Report the malaria status.
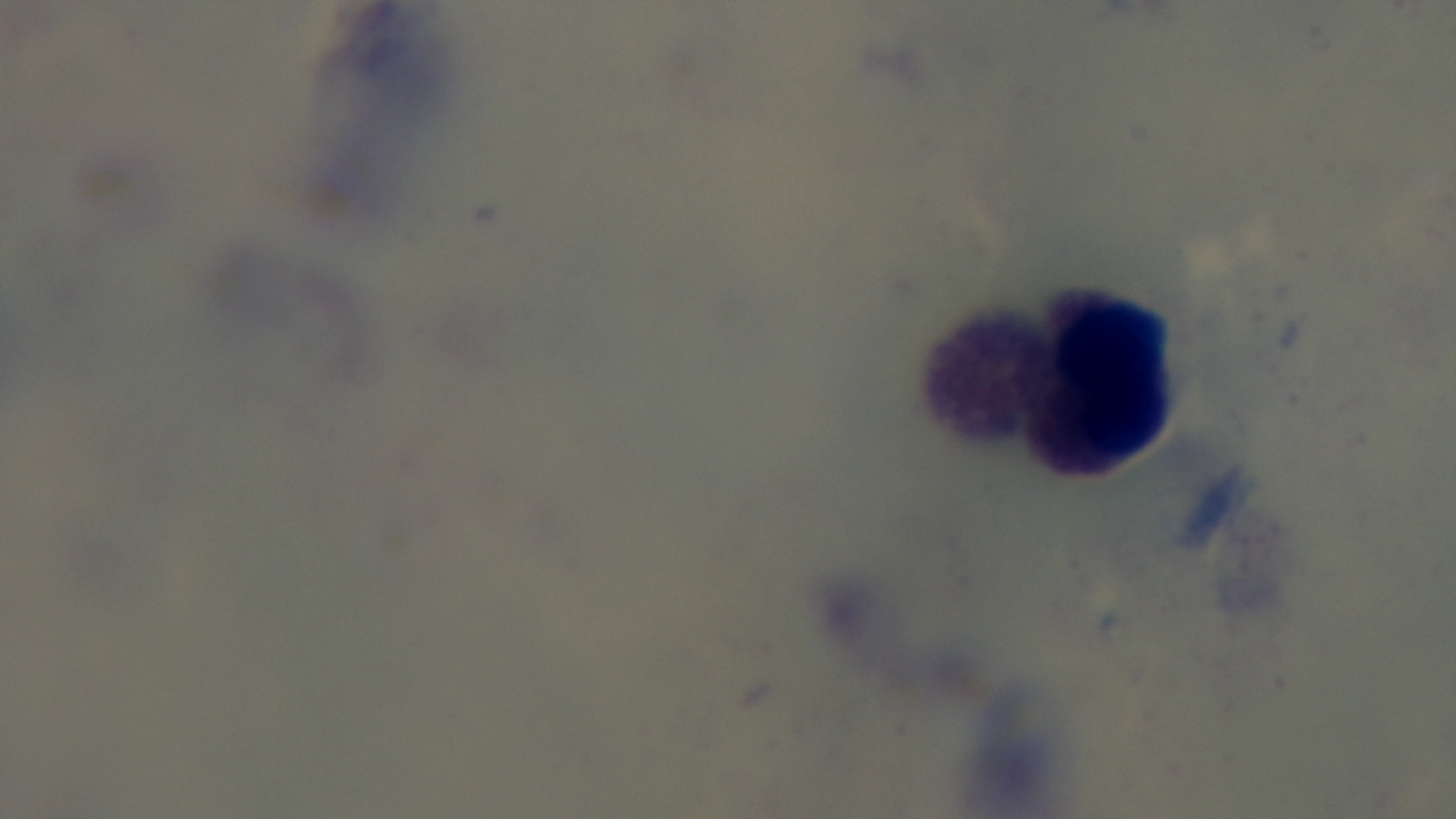

It is uninfected.

Giemsa stain. 100x oil-immersion objective. Photomicrograph. One field from the slide. Captured with a mounted 4K digital camera. Preparation: thick blood film.